State which cell type is depicted.
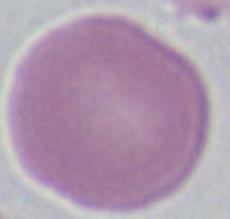

This is an erythrocyte.

Summary:
  - Magnification: 1000x
  - Modality: micrograph